Outline malaria parasites and classify them by life-cycle stage.
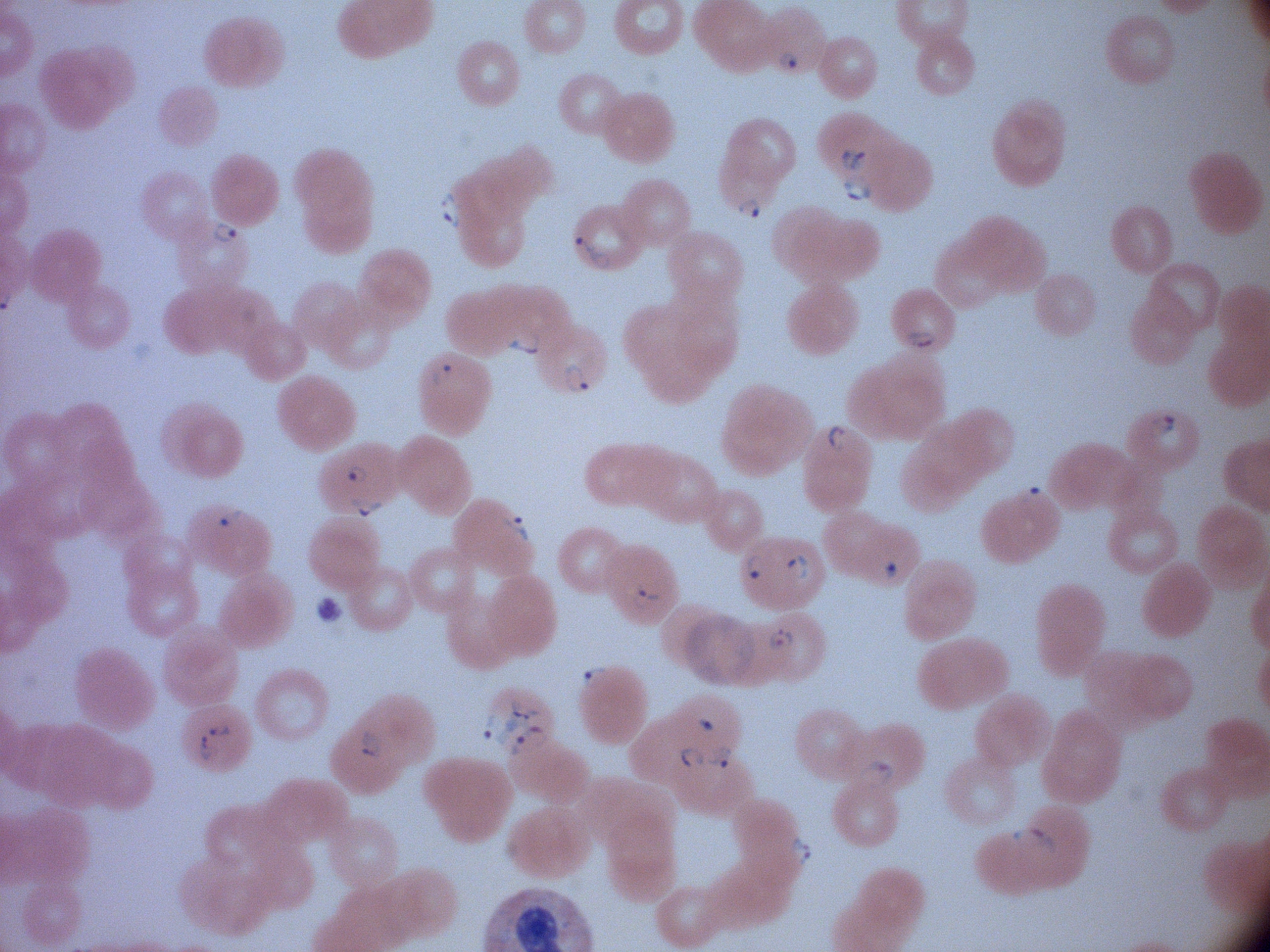

Approximate bounding boxes as [x1, y1, x2, y2] in pixels, from the source annotation, which is not necessarily exhaustive.
Ring forms: [778, 48, 805, 75], [837, 144, 868, 175], [839, 174, 873, 202], [440, 190, 464, 229], [734, 194, 763, 221], [209, 217, 239, 246], [573, 235, 612, 273], [904, 326, 941, 353], [503, 332, 545, 359], [428, 359, 455, 388], [560, 361, 591, 393], [1146, 410, 1179, 441], [823, 423, 849, 456], [343, 461, 369, 485], [347, 493, 385, 516], [215, 503, 246, 528], [501, 510, 532, 542], [740, 553, 770, 586], [784, 553, 811, 582], [629, 581, 661, 610], [767, 625, 796, 651], [579, 663, 611, 696], [476, 693, 557, 760], [692, 712, 721, 735], [204, 721, 236, 742], [355, 727, 391, 762], [192, 731, 220, 763], [707, 744, 739, 775], [679, 747, 707, 769], [858, 757, 896, 789], [1008, 824, 1060, 858], [786, 830, 812, 871].

Giemsa-stained preparation. Acquired with a Leica DM2000 optical microscope and its built-in camera. Image is 1270×952 pixels. 100x magnification. Species: Plasmodium falciparum. One field from this slide. Thin blood film.